Locate every blood parasite and identify its species.
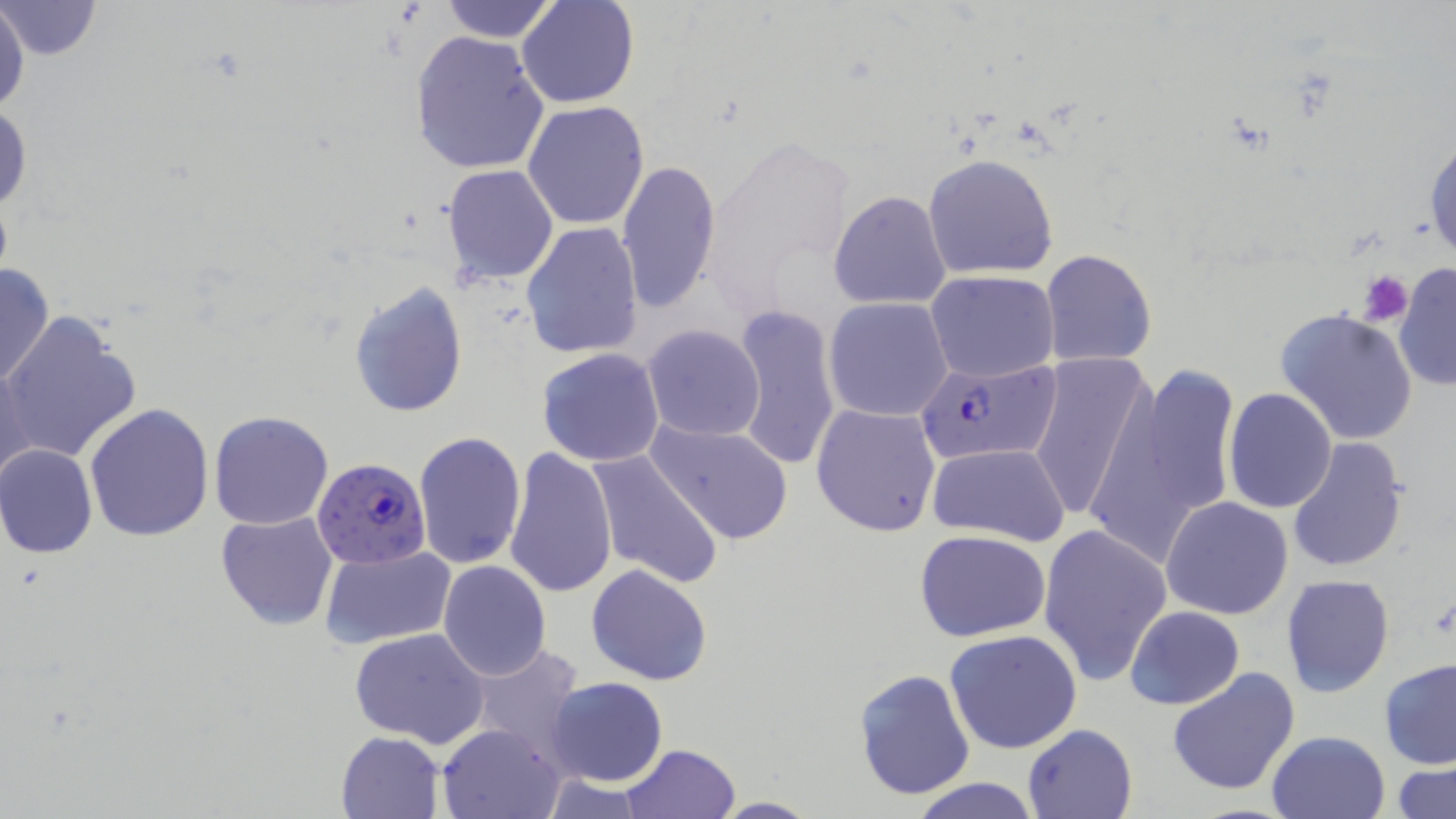
Approximate bounding boxes as (x1, y1, x2, y2) in pixels.
Plasmodium falciparum-infected red blood cells: (914, 362, 1064, 469), (314, 458, 430, 567).
No Plasmodium ovale, Plasmodium malariae, Plasmodium vivax, Babesia divergens, or Trypanosoma brucei observed.

Summary:
  - Uninfected red blood cell locations: (0, 0, 29, 122), (517, 0, 638, 108), (1, 1, 103, 60), (435, 2, 564, 43), (410, 30, 549, 176), (1, 99, 32, 219), (522, 100, 650, 230), (1425, 135, 1456, 266), (923, 153, 1059, 280), (616, 160, 722, 310), (443, 164, 559, 284), (828, 190, 950, 309), (520, 222, 641, 359), (1039, 249, 1158, 368), (0, 263, 53, 390), (1393, 264, 1455, 391), (926, 270, 1058, 381), (348, 280, 469, 416), (824, 297, 954, 422), (731, 306, 840, 471), (1276, 307, 1420, 446), (1, 310, 143, 467), (642, 324, 765, 441), (536, 349, 665, 467), (1026, 354, 1150, 524), (1, 361, 33, 490), (1104, 363, 1237, 549), (1223, 389, 1338, 513), (812, 403, 942, 537), (84, 404, 216, 542), (209, 411, 334, 530), (645, 418, 795, 547), (414, 431, 527, 571), (1287, 437, 1408, 575), (0, 443, 98, 559), (927, 443, 1071, 546), (506, 446, 618, 599), (586, 450, 723, 590), (1160, 496, 1294, 621), (215, 510, 338, 630), (1038, 523, 1173, 686), (914, 530, 1054, 642), (320, 544, 454, 649), (438, 560, 553, 681), (585, 562, 713, 686), (1281, 574, 1395, 697), (1125, 605, 1245, 710), (349, 628, 490, 749), (944, 629, 1083, 755), (462, 642, 582, 765), (1379, 657, 1456, 767), (1166, 665, 1300, 795), (854, 668, 975, 800), (545, 676, 668, 787), (437, 722, 564, 817), (1023, 723, 1137, 818), (1267, 729, 1390, 818), (335, 731, 444, 819), (621, 743, 740, 818), (1391, 761, 1455, 818), (907, 775, 1042, 818), (712, 795, 818, 816)
  - Platelet locations: (1356, 270, 1412, 326)
  - Slide-level diagnosis: Plasmodium falciparum
  - Field of view: single
  - Stain: May-Grünwald-Giemsa
  - Magnification: 1000x
  - Preparation: thin blood film
  - Image size: 1456×819 pixels
  - Modality: optical microscopy